Classify this cell by malaria status.
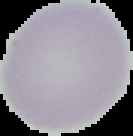

It is uninfected.

image_type: segmented cell region with the area outside set to black
preparation: thin blood film
image_size: 133×136 pixels